Find each parasitized red blood cell.
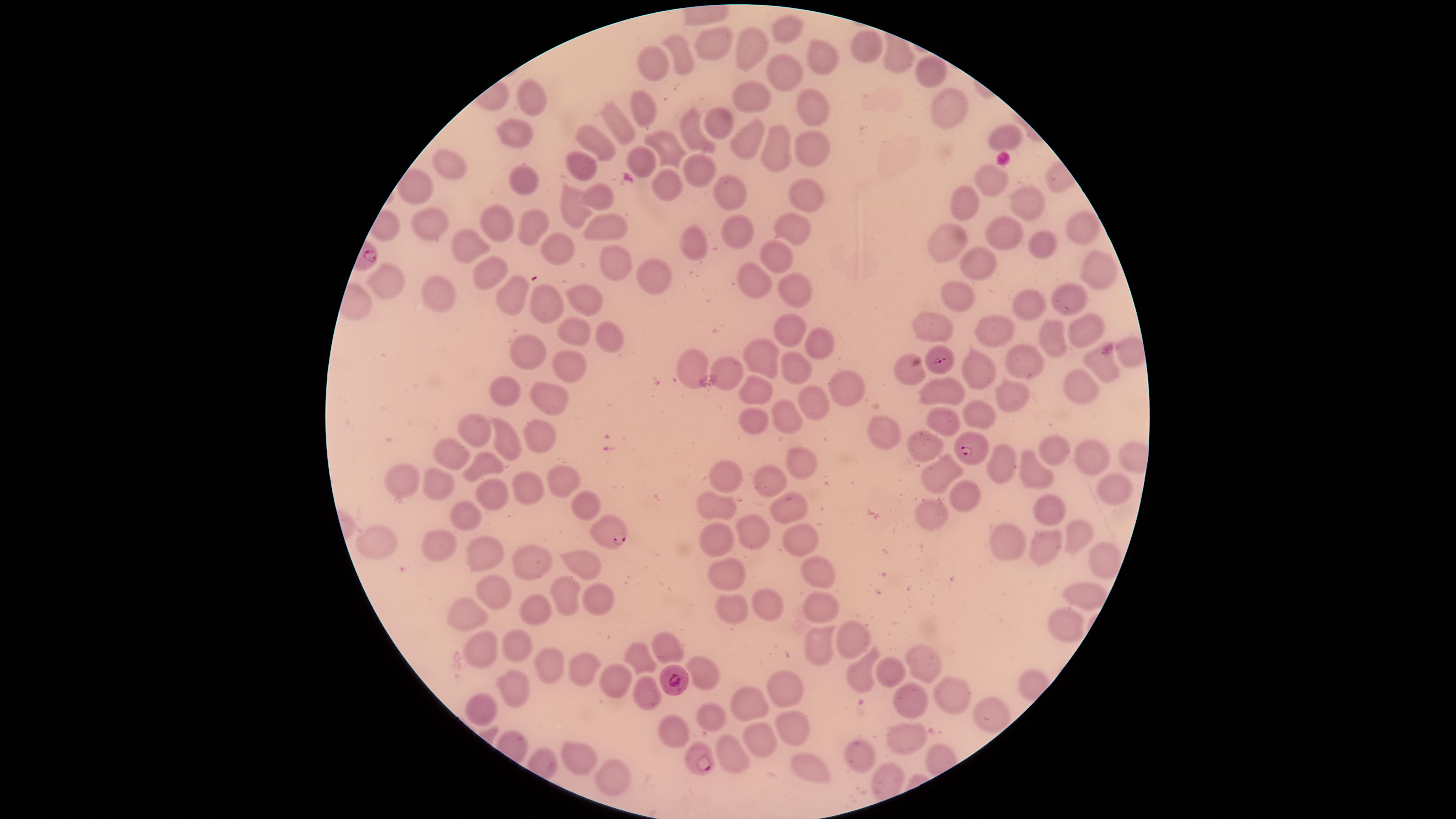
Approximate marker points as (x, y) in pixels.
Parasitized red blood cells: (943, 364), (966, 447), (611, 534), (676, 681), (701, 762).

Approximate marker points as (x, y) in pixels. Uninfected red blood cells: (782, 29), (717, 45), (862, 45), (744, 51), (680, 57), (827, 58), (655, 63), (783, 69), (929, 74), (749, 95), (529, 102), (643, 108), (813, 112), (944, 112), (719, 122), (620, 123), (516, 133), (696, 133), (1009, 134), (601, 144), (749, 144), (813, 145), (780, 146), (675, 147), (643, 158), (700, 164), (587, 166), (455, 168), (670, 178), (989, 178), (522, 182), (730, 193), (597, 197), (811, 197), (1030, 205), (969, 206), (571, 210), (430, 218), (497, 222), (1075, 224), (991, 227), (793, 228), (539, 229), (600, 229), (742, 229), (1037, 242), (692, 243), (946, 246), (561, 247), (470, 250), (778, 261), (616, 263), (974, 263), (1096, 269), (487, 272), (655, 275), (756, 282), (388, 286), (957, 292), (585, 293), (799, 294), (508, 296), (1072, 296), (440, 302), (1034, 306), (542, 307), (1082, 323), (787, 331), (932, 332), (993, 333), (576, 336), (1050, 337), (618, 338), (815, 343), (526, 353), (1132, 353), (762, 355), (565, 362), (689, 363), (1021, 363), (723, 366), (909, 369), (1111, 369), (800, 371), (973, 374), (840, 383), (750, 388), (1083, 392), (942, 393), (543, 397), (502, 398), (1014, 399), (813, 403), (785, 410), (978, 411), (944, 415), (751, 423), (479, 430), (882, 435), (538, 437), (506, 438), (919, 447), (1055, 451), (1091, 456), (448, 461), (471, 464), (802, 464), (996, 466), (950, 473), (1032, 475), (737, 476), (437, 479), (403, 481), (775, 482), (565, 487), (527, 488), (1118, 490), (493, 496), (968, 499), (587, 501), (721, 502), (784, 503), (1045, 503), (461, 512), (937, 516), (753, 530), (1075, 538), (717, 542), (798, 542), (1010, 544), (441, 545), (378, 547), (1046, 547), (476, 553), (527, 558), (1098, 559), (579, 568), (814, 574), (731, 577), (1073, 592), (492, 593), (592, 596), (560, 597), (766, 602), (738, 605), (815, 606), (537, 608), (469, 616), (1065, 624), (819, 641), (520, 646), (857, 648), (665, 649), (482, 654), (641, 659), (922, 662), (554, 665), (581, 667), (862, 672), (710, 673), (885, 674), (613, 681), (514, 684), (781, 686), (647, 689), (905, 699), (950, 699), (481, 703), (750, 706), (714, 715), (994, 717), (792, 727), (757, 738), (678, 739), (905, 742), (577, 753), (730, 753), (859, 761), (807, 769), (607, 772). Thin blood film. Species: Plasmodium falciparum. Image is 1456×819 pixels. Circular visible region. Smartphone photograph through the microscope eyepiece. Single field of view. Giemsa-stained preparation.